Locate every blood parasite and identify its species.
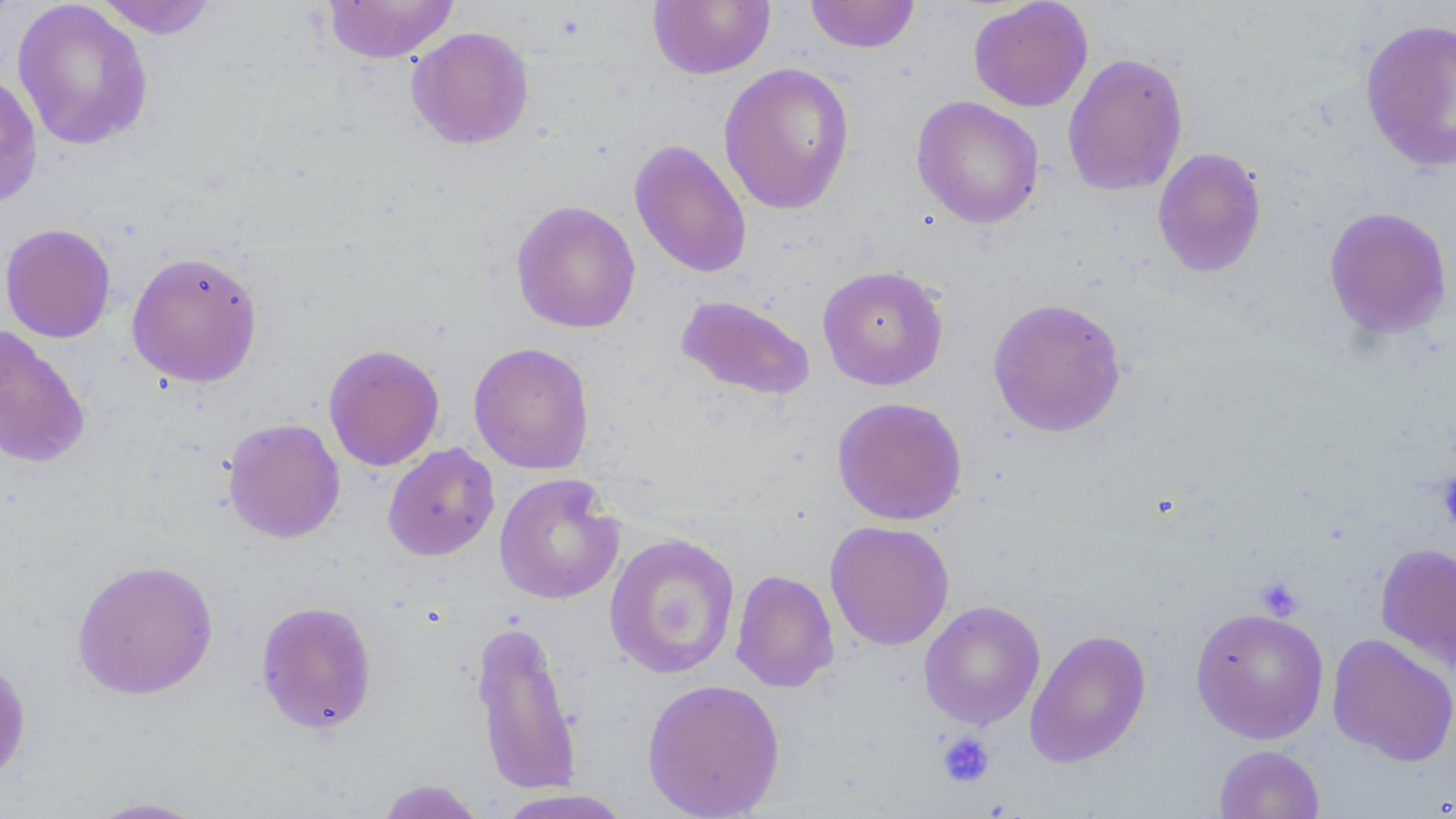
No blood parasites observed.

slide-level diagnosis = no evidence of blood parasites
image size = 1456×819 pixels
modality = light microscopy
field of view = single
preparation = thin blood smear
magnification = 1000x
uninfected red blood cell locations = approximate bounding boxes as (x1, y1, x2, y2) in pixels: (0, 0, 22, 31), (92, 0, 220, 39), (323, 0, 459, 62), (804, 0, 921, 53), (12, 1, 154, 152), (648, 1, 775, 80), (968, 1, 1093, 112), (1360, 18, 1456, 173), (406, 26, 534, 150), (1062, 51, 1188, 196), (718, 62, 855, 215), (0, 71, 43, 209), (911, 96, 1045, 229), (628, 139, 753, 280), (1152, 146, 1268, 278), (511, 199, 641, 334), (1323, 206, 1453, 339), (0, 223, 116, 343), (126, 251, 263, 387), (817, 265, 949, 390), (675, 294, 816, 401), (987, 297, 1127, 438), (0, 325, 91, 469), (468, 341, 595, 475), (323, 342, 445, 471), (831, 396, 968, 526), (222, 417, 345, 544), (382, 443, 500, 562), (494, 472, 624, 605), (825, 520, 955, 651), (604, 532, 740, 680), (1375, 542, 1456, 672), (71, 558, 219, 700), (730, 569, 839, 693), (255, 600, 378, 736), (919, 600, 1045, 730), (1190, 607, 1329, 743), (470, 618, 583, 795), (1024, 629, 1151, 768), (1327, 634, 1456, 766), (0, 654, 32, 787), (642, 677, 785, 819), (1214, 744, 1325, 819), (374, 778, 490, 819), (494, 789, 635, 819), (85, 796, 213, 818)
stain = May-Grünwald-Giemsa
platelet locations = approximate bounding boxes as (x1, y1, x2, y2) in pixels: (1438, 471, 1456, 531), (1255, 577, 1304, 620), (936, 731, 995, 789)